Name the parasite shown.
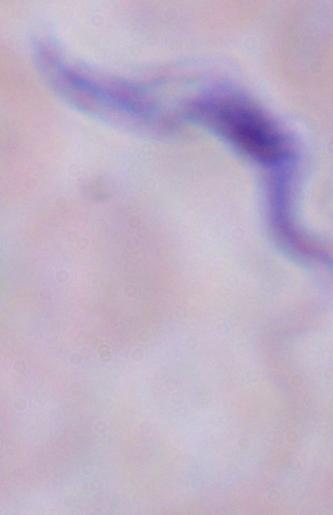

A trypanosome.

Captured at 1000x magnification. Photomicrograph.